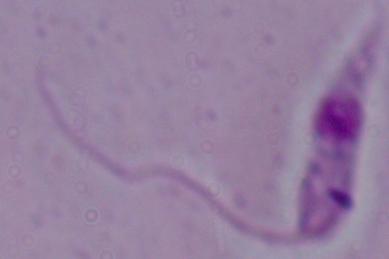

modality = photomicrograph
magnification = 1000x
identification = Leishmania